Identify the blood parasite species.
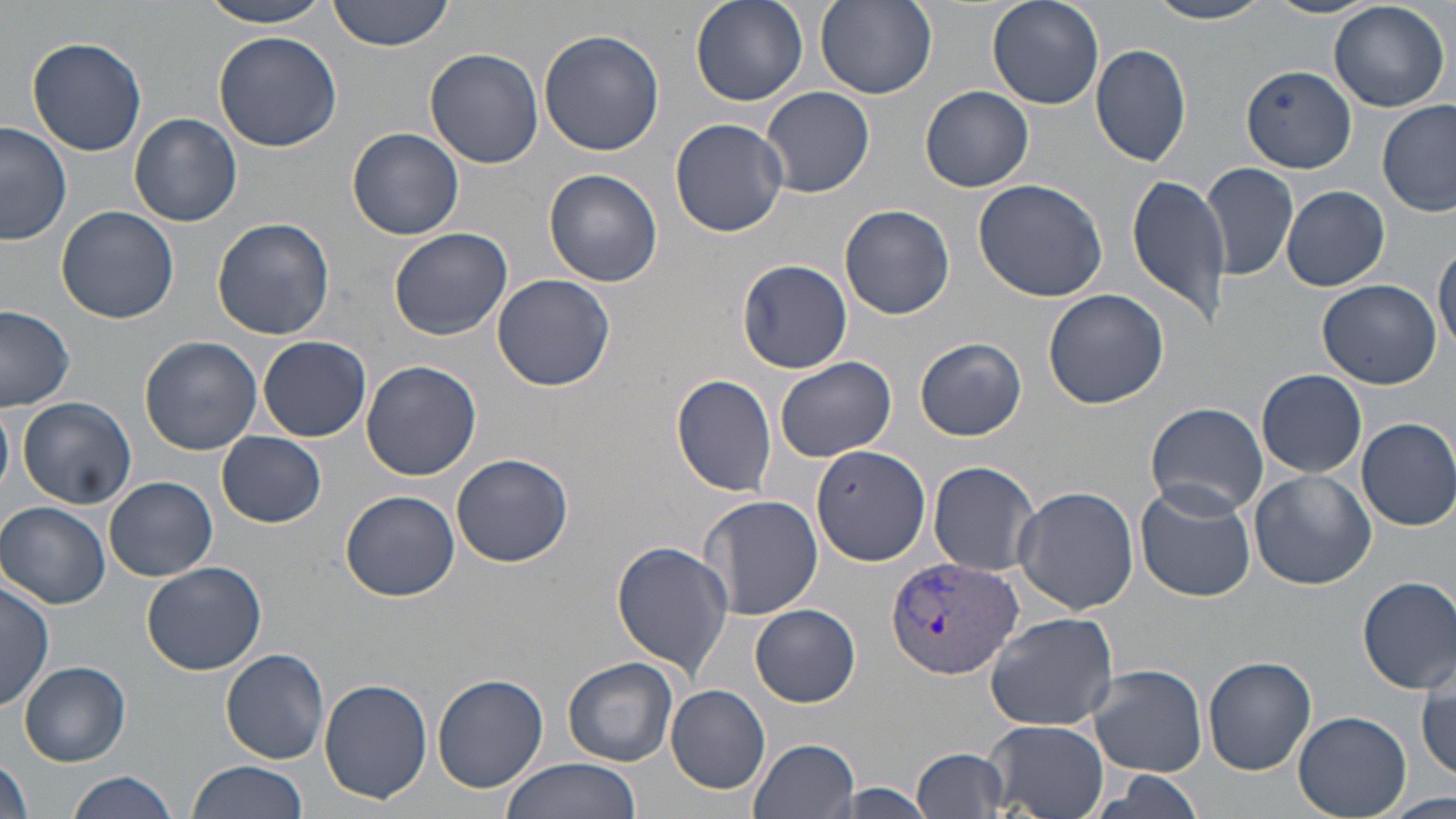

Plasmodium vivax.

{
  "modality": "light microscopy",
  "image_size": "1456×819 pixels",
  "magnification": "1000x",
  "field_of_view": "single",
  "stain": "May-Grünwald-Giemsa",
  "preparation": "thin blood film",
  "plasmodium_vivax_infected_red_blood_cell_locations": "approximate bounding boxes as named x1/y1/x2/y2 corners in pixels: (x1=884, y1=557, x2=1025, y2=681)",
  "uninfected_red_blood_cell_locations": "approximate bounding boxes as named x1/y1/x2/y2 corners in pixels: (x1=195, y1=0, x2=342, y2=29), (x1=331, y1=0, x2=457, y2=51), (x1=691, y1=0, x2=808, y2=108), (x1=987, y1=0, x2=1104, y2=110), (x1=1263, y1=0, x2=1382, y2=19), (x1=815, y1=1, x2=939, y2=100), (x1=1146, y1=1, x2=1274, y2=25), (x1=1329, y1=1, x2=1449, y2=112), (x1=212, y1=29, x2=345, y2=152), (x1=538, y1=29, x2=664, y2=157), (x1=26, y1=35, x2=147, y2=156), (x1=1091, y1=42, x2=1192, y2=168), (x1=425, y1=47, x2=545, y2=169), (x1=1242, y1=65, x2=1355, y2=173), (x1=762, y1=86, x2=875, y2=198), (x1=921, y1=86, x2=1033, y2=192), (x1=1378, y1=98, x2=1456, y2=218), (x1=129, y1=112, x2=242, y2=226), (x1=670, y1=118, x2=789, y2=238), (x1=0, y1=121, x2=74, y2=247), (x1=348, y1=127, x2=464, y2=240), (x1=1203, y1=161, x2=1299, y2=282), (x1=544, y1=169, x2=663, y2=288), (x1=1126, y1=171, x2=1232, y2=327), (x1=973, y1=178, x2=1108, y2=303), (x1=1281, y1=186, x2=1391, y2=292), (x1=839, y1=204, x2=956, y2=320), (x1=56, y1=206, x2=181, y2=324), (x1=212, y1=217, x2=335, y2=340), (x1=388, y1=227, x2=512, y2=340), (x1=1432, y1=237, x2=1456, y2=358), (x1=740, y1=259, x2=852, y2=372), (x1=490, y1=273, x2=616, y2=391), (x1=1316, y1=279, x2=1442, y2=388), (x1=1042, y1=288, x2=1169, y2=409), (x1=0, y1=305, x2=75, y2=411), (x1=258, y1=335, x2=371, y2=442), (x1=139, y1=336, x2=262, y2=455), (x1=916, y1=338, x2=1026, y2=441), (x1=360, y1=359, x2=483, y2=480), (x1=776, y1=360, x2=896, y2=461), (x1=1256, y1=367, x2=1368, y2=478), (x1=671, y1=374, x2=778, y2=496), (x1=16, y1=396, x2=137, y2=510), (x1=1146, y1=402, x2=1271, y2=516), (x1=0, y1=406, x2=14, y2=500), (x1=1355, y1=417, x2=1456, y2=531), (x1=217, y1=432, x2=326, y2=528), (x1=812, y1=440, x2=930, y2=566), (x1=450, y1=452, x2=576, y2=569), (x1=927, y1=461, x2=1043, y2=575), (x1=1249, y1=469, x2=1377, y2=590), (x1=103, y1=475, x2=217, y2=581), (x1=1135, y1=482, x2=1255, y2=601), (x1=1013, y1=485, x2=1139, y2=614), (x1=339, y1=490, x2=461, y2=603), (x1=699, y1=493, x2=823, y2=623), (x1=1, y1=502, x2=111, y2=610), (x1=611, y1=540, x2=733, y2=676), (x1=141, y1=561, x2=268, y2=676), (x1=1357, y1=575, x2=1456, y2=692), (x1=1, y1=579, x2=53, y2=710), (x1=751, y1=603, x2=861, y2=707), (x1=984, y1=610, x2=1120, y2=732), (x1=222, y1=649, x2=331, y2=763), (x1=1204, y1=656, x2=1317, y2=774), (x1=563, y1=657, x2=678, y2=766), (x1=18, y1=661, x2=131, y2=767), (x1=1088, y1=663, x2=1207, y2=776), (x1=1415, y1=664, x2=1455, y2=782), (x1=431, y1=674, x2=548, y2=792), (x1=319, y1=680, x2=432, y2=804), (x1=667, y1=685, x2=770, y2=792), (x1=1294, y1=711, x2=1410, y2=818), (x1=983, y1=720, x2=1108, y2=819), (x1=748, y1=737, x2=860, y2=819), (x1=913, y1=747, x2=1009, y2=816), (x1=1, y1=756, x2=35, y2=819), (x1=501, y1=757, x2=642, y2=818), (x1=186, y1=758, x2=310, y2=819), (x1=66, y1=770, x2=179, y2=819), (x1=830, y1=784, x2=939, y2=819), (x1=1385, y1=791, x2=1455, y2=819)"
}